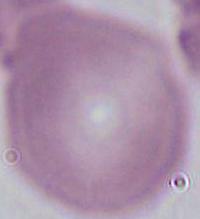
Summary:
  - Magnification: 1000x
  - Identification: erythrocyte
  - Modality: photomicrograph